Classify this cell by malaria status.
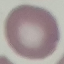
Uninfected.

Giemsa stain. Acquired by smartphone through the microscope eyepiece. Thin smear of blood. Cell patch, automatically extracted from a larger field of view and resized to 64 × 64 pixels.